Assess this cell for malaria.
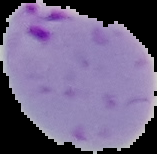
It is parasitized.

Image is 157×154 pixels. From a thin blood film. Cell region segmented out of the field of view; the surrounding area is masked to black.